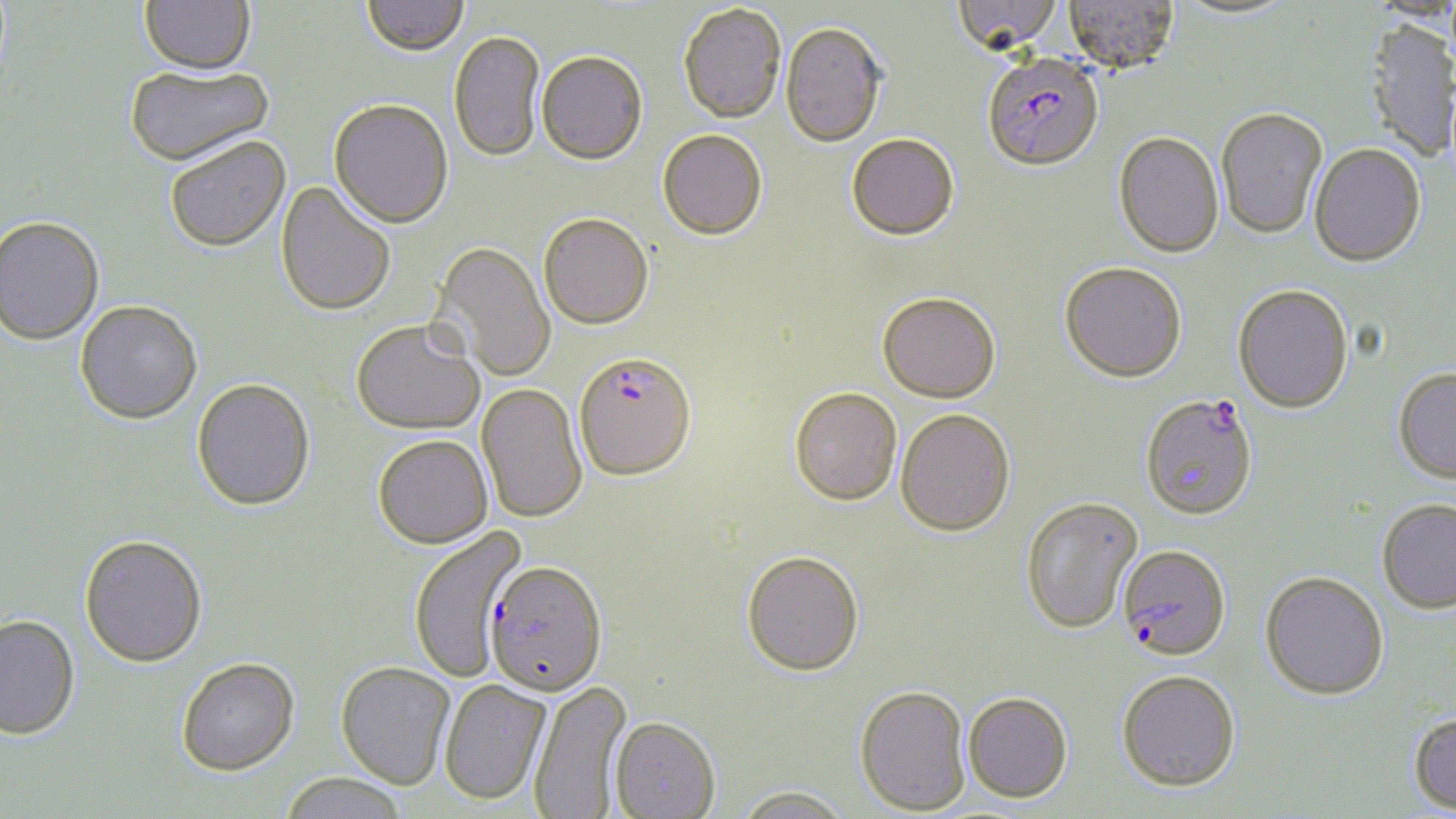 Approximate bounding boxes as (x1, y1, x2, y2) in pixels. Plasmodium falciparum-infected red blood cell locations: (983, 55, 1103, 173), (573, 352, 698, 482), (1140, 393, 1259, 520), (1118, 544, 1231, 660), (485, 562, 607, 700). Uninfected red blood cell locations: (139, 0, 256, 79), (362, 0, 468, 59), (950, 0, 1065, 56), (1064, 0, 1179, 74), (1171, 1, 1300, 21), (678, 5, 786, 126), (1362, 19, 1454, 164), (780, 25, 885, 149), (449, 32, 545, 164), (536, 54, 647, 168), (125, 66, 276, 169), (328, 101, 453, 231), (1216, 107, 1328, 239), (658, 131, 767, 242), (1114, 131, 1224, 258), (847, 136, 959, 243), (166, 138, 291, 255), (1310, 143, 1426, 267), (275, 181, 395, 319), (538, 216, 654, 332), (0, 218, 104, 347), (430, 242, 555, 381), (1059, 262, 1187, 383), (1232, 285, 1354, 414), (877, 294, 1001, 405), (75, 302, 203, 427), (351, 322, 485, 437), (1393, 367, 1456, 483), (191, 380, 316, 513), (476, 384, 587, 524), (789, 389, 902, 509), (895, 410, 1015, 538), (372, 437, 493, 550), (1021, 496, 1144, 633), (1377, 499, 1456, 614), (408, 527, 527, 683), (79, 537, 207, 670), (741, 553, 864, 679), (1260, 571, 1388, 699), (0, 614, 80, 741), (177, 661, 300, 779), (336, 663, 455, 791), (1116, 670, 1241, 791), (439, 680, 552, 807), (530, 682, 633, 819), (854, 687, 972, 816), (963, 692, 1073, 804), (1407, 712, 1456, 814), (609, 720, 721, 819), (278, 774, 408, 819), (732, 787, 855, 819). Slide-level diagnosis: Plasmodium falciparum. Thin blood film. Single field of view. May-Grünwald-Giemsa stain. Light microscopy. 1000x magnification. Image is 1456×819 pixels.